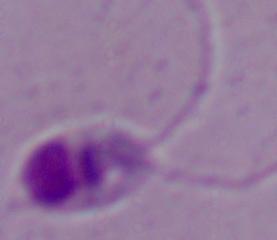

magnification = 1000x
identification = Leishmania
modality = photomicrograph